State the blood parasite species.
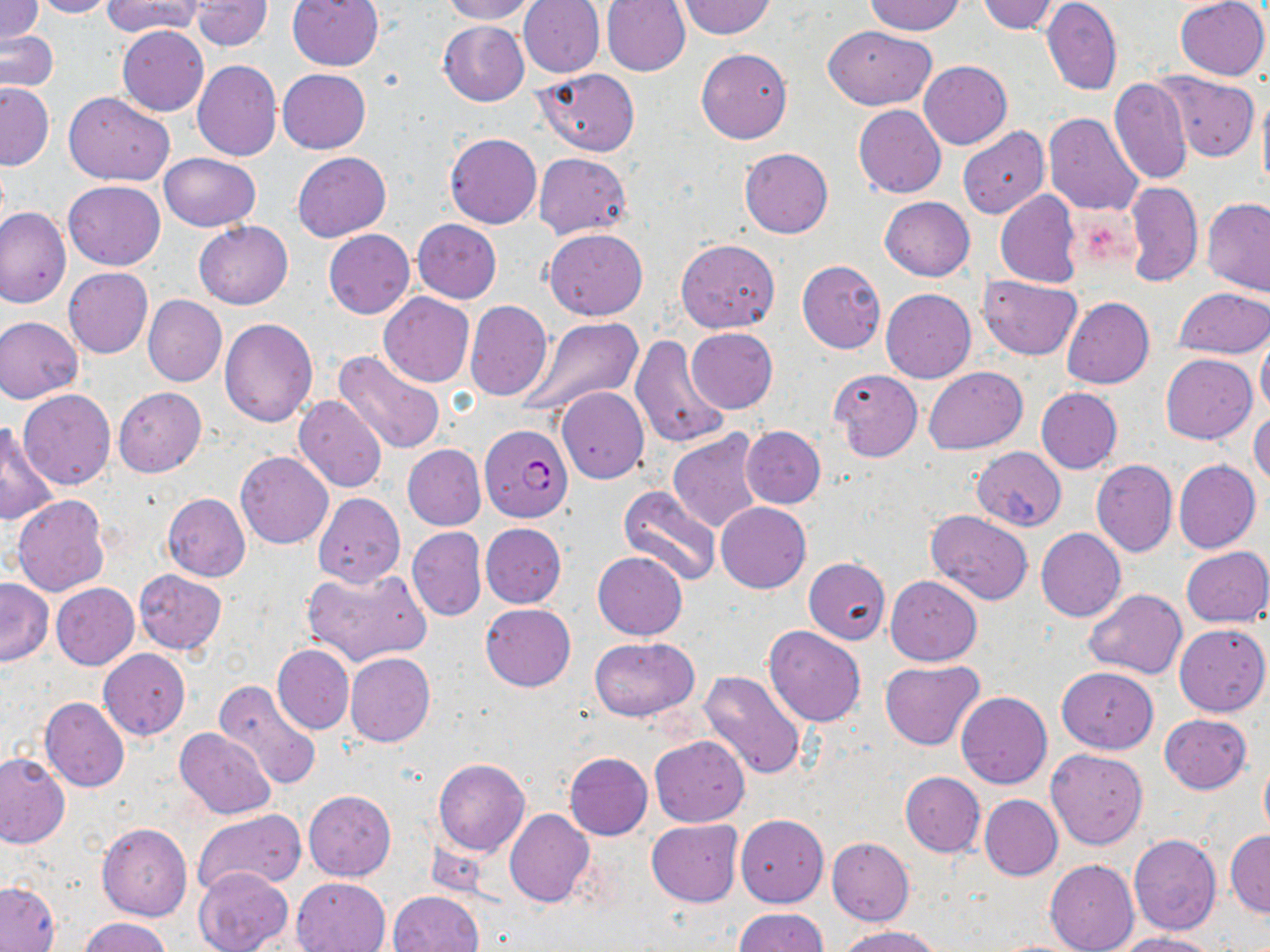
Plasmodium falciparum.

Approximate bounding boxes as [x1, y1, x2, y2] in pixels. Uninfected red blood cell locations: [0, 0, 42, 45], [30, 0, 115, 18], [101, 0, 205, 37], [191, 0, 271, 51], [288, 0, 384, 71], [438, 0, 536, 24], [517, 0, 605, 77], [865, 0, 966, 35], [975, 0, 1060, 35], [1042, 0, 1122, 96], [1174, 0, 1269, 80], [601, 1, 691, 76], [678, 1, 777, 39], [438, 19, 529, 106], [117, 25, 209, 115], [823, 25, 936, 109], [0, 30, 58, 93], [696, 47, 792, 144], [192, 59, 282, 161], [919, 60, 1011, 149], [276, 69, 370, 154], [537, 69, 640, 155], [1153, 71, 1260, 162], [1109, 79, 1192, 184], [0, 83, 53, 170], [1257, 88, 1270, 198], [63, 92, 175, 185], [853, 105, 946, 198], [1043, 112, 1144, 215], [957, 126, 1049, 219], [444, 133, 541, 229], [740, 148, 833, 239], [158, 152, 260, 230], [292, 152, 391, 241], [533, 152, 631, 240], [1125, 180, 1203, 288], [63, 181, 164, 270], [994, 190, 1082, 289], [879, 197, 974, 281], [1200, 197, 1270, 297], [0, 207, 70, 309], [412, 219, 501, 303], [193, 221, 293, 309], [323, 229, 415, 319], [544, 229, 648, 320], [675, 239, 779, 332], [797, 259, 886, 354], [63, 268, 152, 358], [980, 274, 1082, 358], [1173, 287, 1268, 358], [881, 289, 975, 382], [378, 292, 474, 387], [143, 295, 226, 386], [1061, 297, 1154, 389], [464, 300, 553, 401], [1, 315, 84, 403], [522, 317, 643, 417], [219, 318, 318, 427], [687, 328, 778, 413], [629, 334, 732, 449], [1256, 334, 1270, 420], [333, 350, 447, 455], [1161, 353, 1256, 443], [924, 366, 1027, 453], [829, 369, 922, 461], [113, 387, 206, 477], [557, 387, 649, 484], [1036, 388, 1122, 474], [18, 390, 116, 489], [294, 395, 388, 494], [1249, 409, 1270, 488], [1, 424, 60, 525], [740, 426, 825, 508], [668, 430, 765, 534], [403, 445, 486, 531], [971, 447, 1066, 532], [235, 452, 333, 549], [1091, 460, 1177, 558], [1174, 460, 1260, 553], [171, 477, 325, 573], [617, 484, 722, 588], [162, 493, 251, 581], [312, 493, 405, 588], [12, 495, 109, 596], [716, 502, 810, 592], [925, 511, 1034, 606], [480, 523, 566, 607], [407, 526, 486, 622], [1036, 528, 1126, 621], [1181, 546, 1270, 627], [592, 552, 687, 640], [803, 558, 890, 644], [303, 565, 432, 668], [134, 570, 226, 655], [886, 575, 982, 666], [0, 579, 53, 667], [51, 583, 140, 670], [1085, 589, 1187, 677], [479, 603, 576, 691], [1175, 623, 1269, 717], [763, 626, 866, 726], [590, 636, 699, 720], [273, 644, 354, 734], [99, 648, 190, 740], [345, 652, 435, 747], [879, 659, 984, 751], [1056, 667, 1159, 753], [698, 670, 807, 782], [212, 678, 323, 790], [956, 692, 1052, 789], [39, 697, 129, 793], [1159, 714, 1252, 794], [176, 728, 276, 819], [649, 734, 750, 827], [1046, 748, 1150, 849], [564, 752, 652, 840], [0, 753, 69, 847], [432, 758, 529, 855], [1260, 758, 1270, 836], [899, 771, 985, 857], [304, 789, 396, 880], [979, 794, 1062, 880], [192, 810, 304, 898], [504, 810, 594, 909], [736, 814, 828, 908], [647, 819, 742, 906], [97, 823, 192, 921], [1226, 830, 1270, 917], [1129, 835, 1222, 935], [826, 838, 914, 925], [1045, 859, 1139, 952], [194, 867, 293, 952], [292, 876, 391, 951], [1, 880, 59, 952], [388, 891, 484, 952], [734, 908, 829, 952], [78, 916, 171, 952], [839, 925, 943, 952], [1113, 932, 1220, 952]. Platelet locations: [1074, 212, 1136, 268]. Plasmodium falciparum-infected red blood cell locations: [480, 423, 572, 521]. Image is 1270×952 pixels. One field of a larger specimen. 1000x magnification. Thin blood film. Optical microscopy. May-Grünwald-Giemsa-stained preparation.